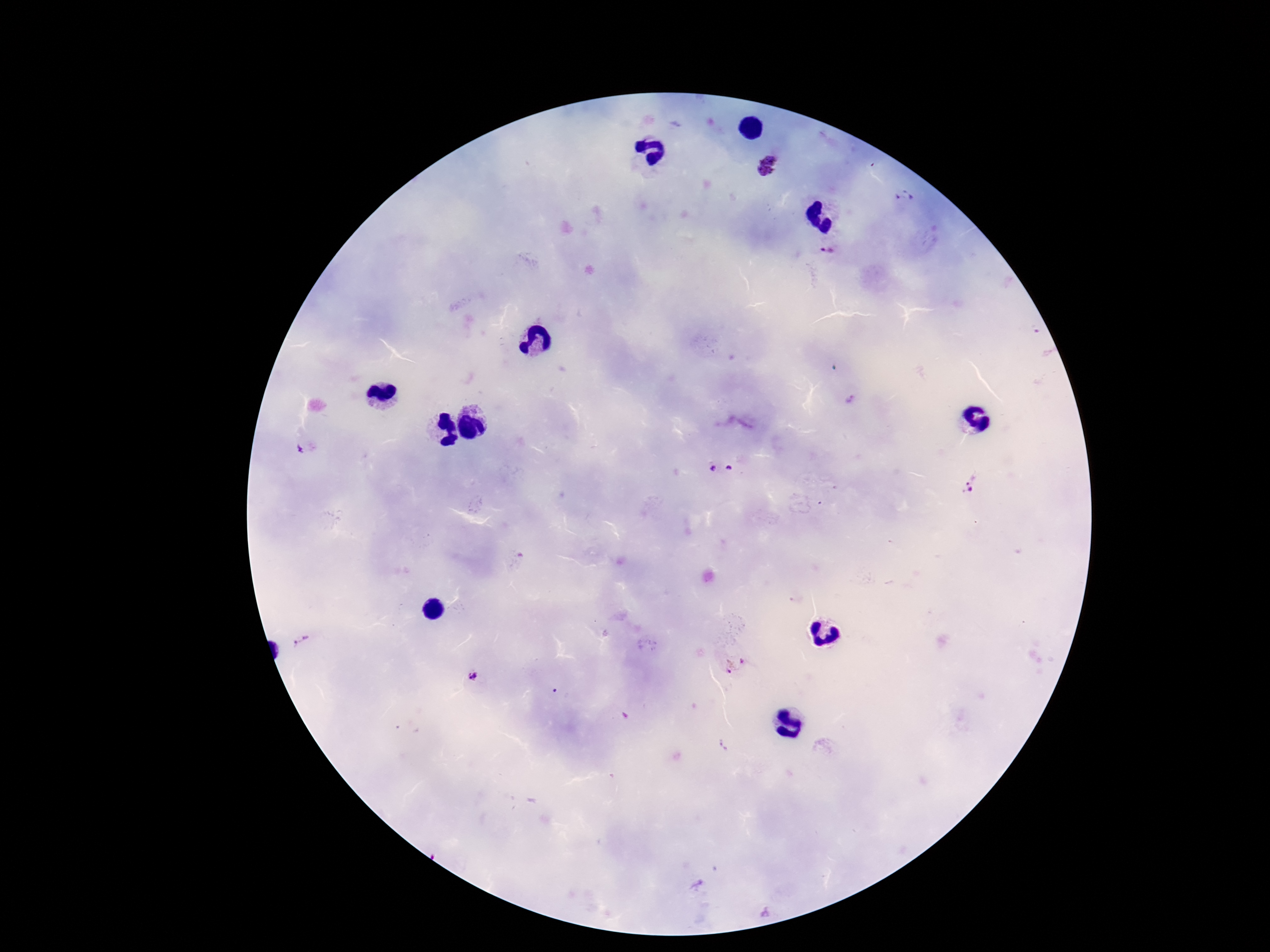
stain = Giemsa
patient malaria status = infected
field of view = single
preparation = thick blood film
Plasmodium parasite locations = approximate centers as [x, y] in pixels: [767, 164], [905, 198], [828, 252], [713, 466], [729, 468], [971, 482], [303, 639], [735, 664], [473, 678]
magnification = 100x
image size = 1270×952 pixels
capture = smartphone camera through the microscope eyepiece